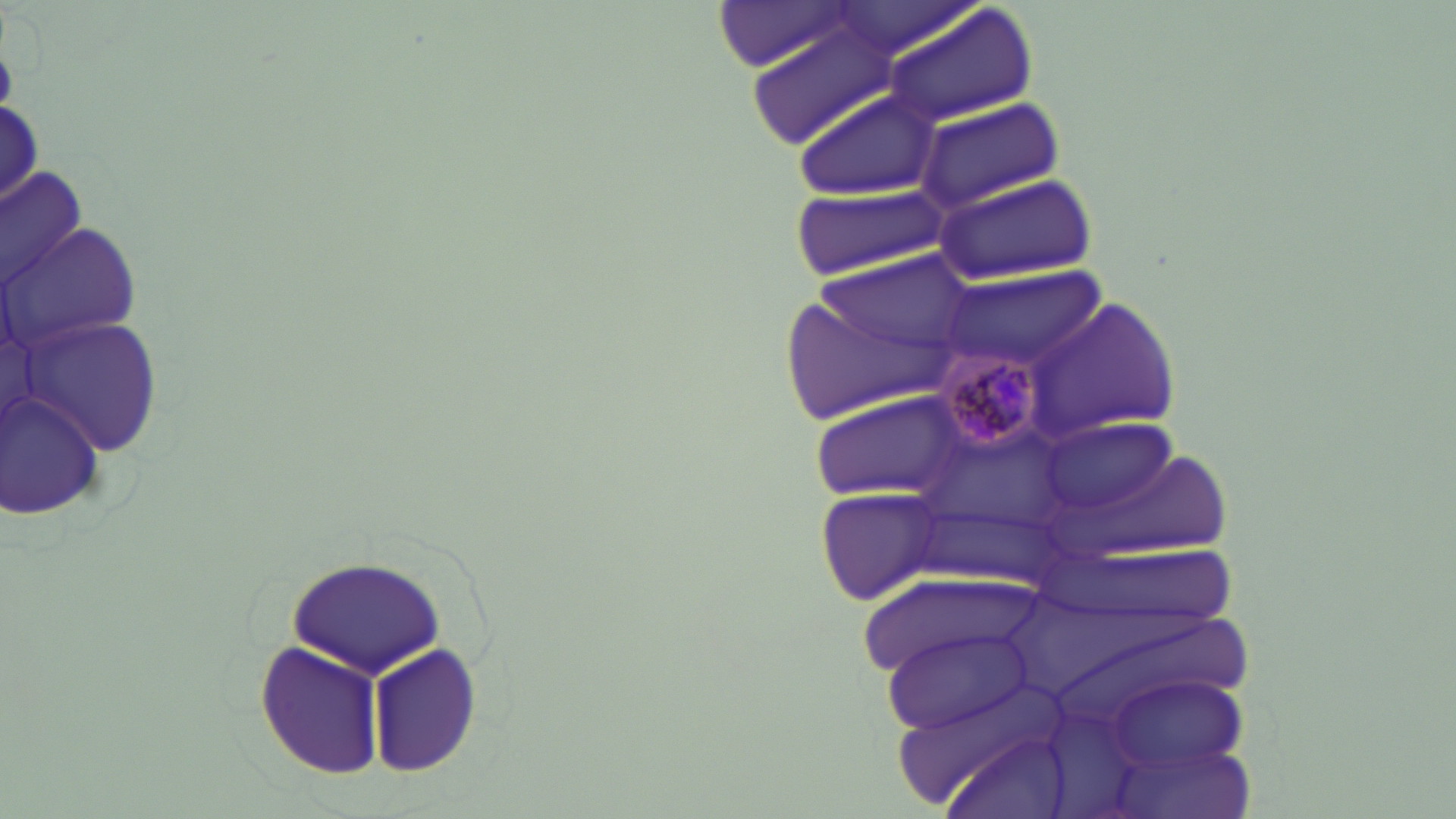 Approximate bounding boxes as (x1,y1)-(x2,y2) corner pairs in pixels. Plasmodium malariae-infected red blood cell locations: (931,348)-(1053,458). Uninfected red blood cell locations: (714,1)-(860,72), (821,1)-(981,62), (882,5)-(1038,130), (751,19)-(907,152), (793,88)-(941,198), (916,99)-(1067,212), (1,166)-(87,291), (932,171)-(1102,287), (794,183)-(953,279), (10,198)-(146,378), (799,249)-(979,388), (939,266)-(1109,377), (1029,297)-(1179,441), (24,311)-(171,461), (0,389)-(109,520), (809,392)-(972,503), (1038,411)-(1187,534), (815,486)-(950,606), (289,556)-(449,679), (880,627)-(1031,731), (255,643)-(385,778), (368,645)-(481,774). Slide-level diagnosis: Plasmodium malariae. Single field of view. May-Grünwald-Giemsa stain. Image is 1456×819 pixels. Thin blood smear. Optical microscopy. 1000x magnification.